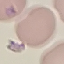

malaria status = parasitized
capture = smartphone camera at the microscope eyepiece
image type = automatically extracted cell patch, resized to 64 × 64 pixels
preparation = thin blood smear
stain = Giemsa